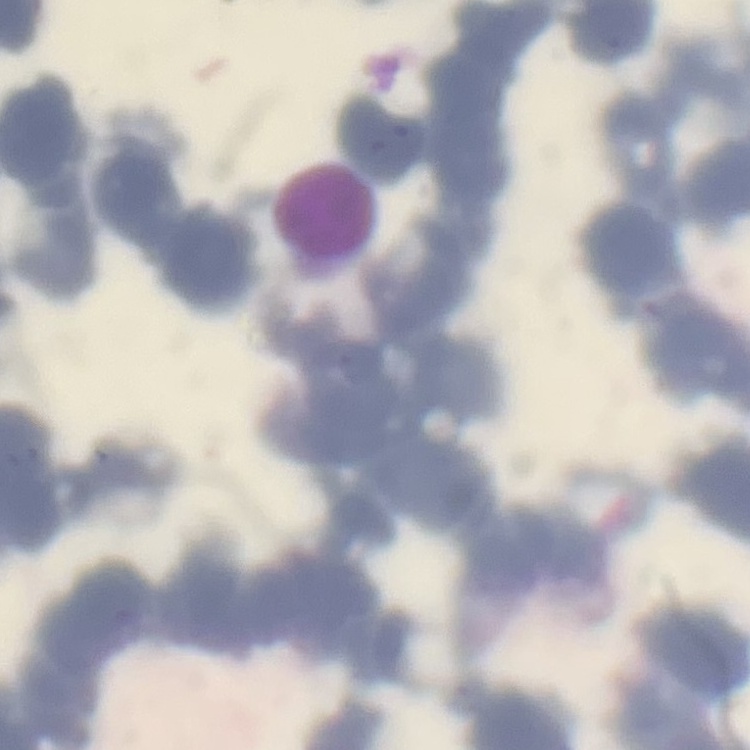
Summary:
  - Red blood cell morphology: rouleaux formation
  - Preparation: thin peripheral smear
  - Stain: Field's or Giemsa
  - Image type: square crop of a larger photomicrograph